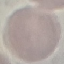
malaria status = uninfected
preparation = thin smear
stain = Giemsa
image type = automatically extracted cell patch, resized to 64 × 64 pixels
capture = smartphone camera at the microscope eyepiece